State the preparation type.
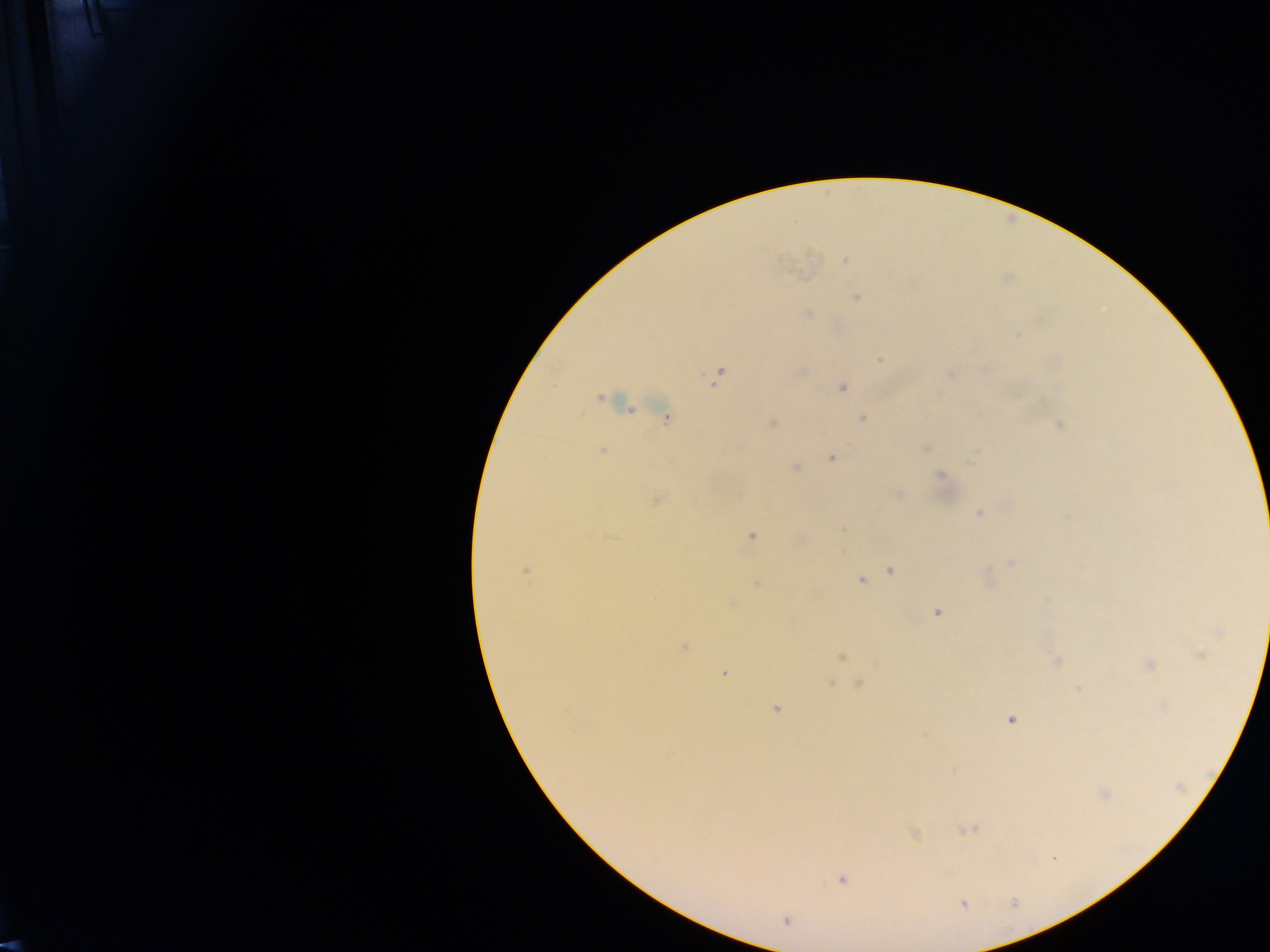

Thick blood smear.

field of view = single
capture = mobile-phone photograph through a microscope
Plasmodium parasite locations = approximate centers as [x, y] in pixels: [844, 260], [855, 297], [808, 314], [1017, 334], [880, 360], [718, 376], [842, 388], [600, 398], [666, 417], [862, 419], [772, 423], [1059, 425], [925, 448], [602, 451], [832, 458], [796, 468], [941, 474], [898, 493], [657, 500], [978, 513], [843, 531], [751, 536], [1011, 563], [525, 571], [891, 571], [861, 581], [938, 612], [1219, 633], [685, 648], [842, 657], [1056, 661], [1149, 665], [724, 674], [859, 683], [776, 709], [1011, 719], [925, 735], [1105, 793], [967, 830], [914, 833], [842, 880], [964, 904], [786, 921]
image size = 1270×952 pixels
country = Ghana